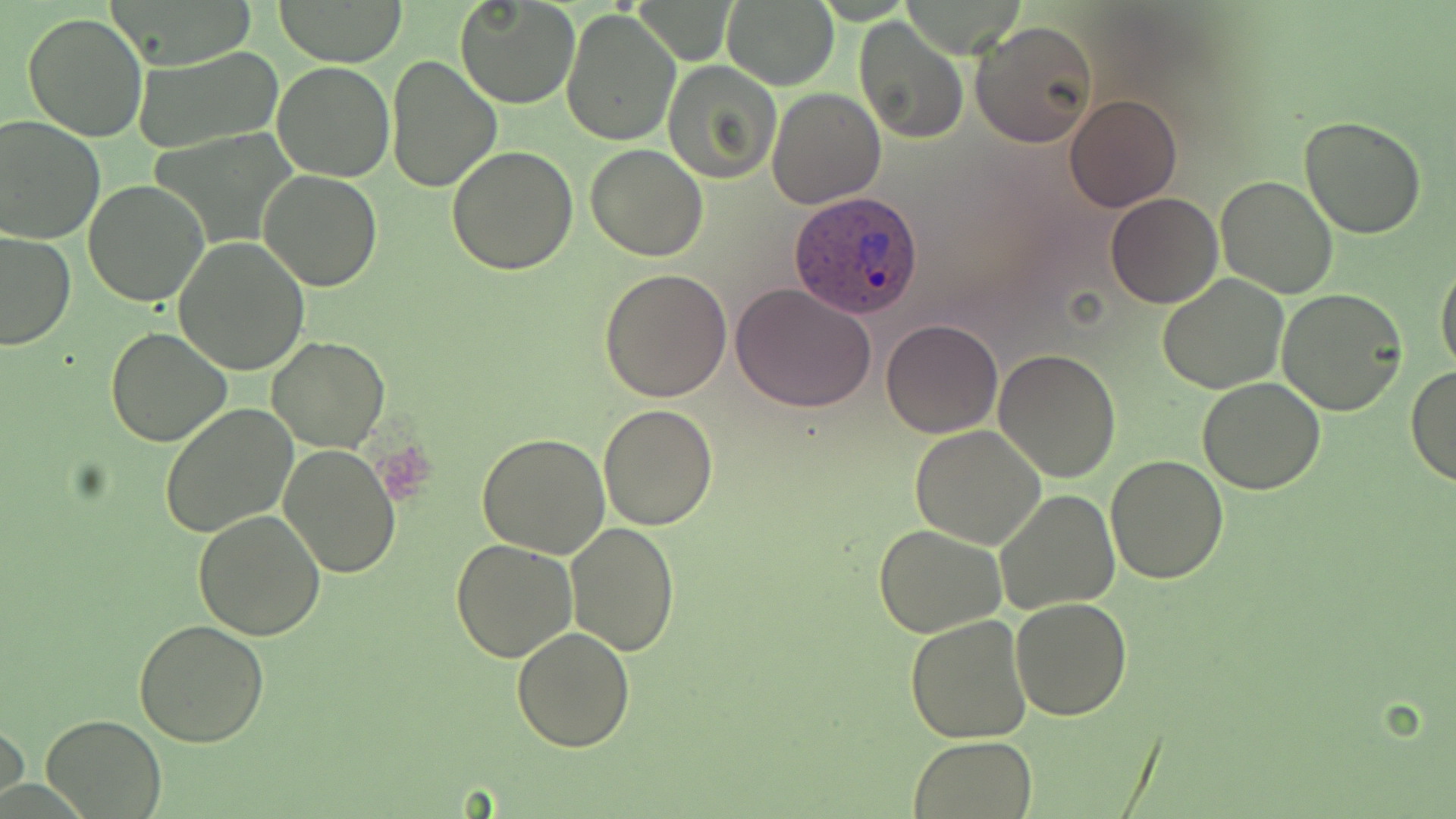 Approximate bounding boxes as named x1/y1/x2/y2 corners in pixels. Uninfected red blood cell locations: (x1=276, y1=0, x2=406, y2=66), (x1=454, y1=1, x2=580, y2=109), (x1=722, y1=2, x2=839, y2=88), (x1=560, y1=6, x2=682, y2=146), (x1=21, y1=12, x2=148, y2=142), (x1=854, y1=16, x2=970, y2=146), (x1=971, y1=20, x2=1099, y2=148), (x1=132, y1=47, x2=283, y2=155), (x1=385, y1=56, x2=500, y2=192), (x1=663, y1=61, x2=781, y2=184), (x1=272, y1=63, x2=395, y2=183), (x1=768, y1=87, x2=885, y2=208), (x1=1063, y1=93, x2=1183, y2=212), (x1=0, y1=115, x2=105, y2=244), (x1=1300, y1=116, x2=1427, y2=239), (x1=586, y1=143, x2=707, y2=260), (x1=446, y1=145, x2=579, y2=275), (x1=259, y1=170, x2=383, y2=294), (x1=1215, y1=175, x2=1340, y2=299), (x1=84, y1=181, x2=210, y2=306), (x1=1105, y1=192, x2=1223, y2=308), (x1=0, y1=230, x2=74, y2=351), (x1=175, y1=238, x2=310, y2=375), (x1=1435, y1=255, x2=1456, y2=379), (x1=599, y1=267, x2=732, y2=402), (x1=1156, y1=273, x2=1290, y2=393), (x1=731, y1=283, x2=879, y2=412), (x1=1276, y1=288, x2=1407, y2=416), (x1=881, y1=319, x2=1002, y2=438), (x1=105, y1=326, x2=232, y2=448), (x1=266, y1=336, x2=390, y2=452), (x1=993, y1=348, x2=1124, y2=484), (x1=1405, y1=365, x2=1456, y2=487), (x1=1197, y1=376, x2=1326, y2=494), (x1=158, y1=402, x2=297, y2=540), (x1=599, y1=402, x2=719, y2=531), (x1=911, y1=425, x2=1045, y2=550), (x1=475, y1=432, x2=609, y2=559), (x1=280, y1=443, x2=401, y2=577), (x1=1105, y1=455, x2=1229, y2=584), (x1=995, y1=490, x2=1118, y2=613), (x1=192, y1=510, x2=325, y2=642), (x1=566, y1=522, x2=679, y2=657), (x1=874, y1=524, x2=1006, y2=638), (x1=451, y1=538, x2=578, y2=663), (x1=1009, y1=597, x2=1132, y2=720), (x1=904, y1=615, x2=1033, y2=742), (x1=133, y1=619, x2=270, y2=748), (x1=512, y1=627, x2=635, y2=752), (x1=1, y1=713, x2=27, y2=809), (x1=41, y1=714, x2=166, y2=819), (x1=906, y1=737, x2=1039, y2=818). Plasmodium ovale-infected red blood cell locations: (x1=788, y1=190, x2=924, y2=320). Slide-level diagnosis: Plasmodium ovale. Image is 1456×819 pixels. Single field of view. 1000x magnification. Thin blood smear. May-Grünwald-Giemsa-stained preparation. Optical microscopy.